Point out each Plasmodium parasite.
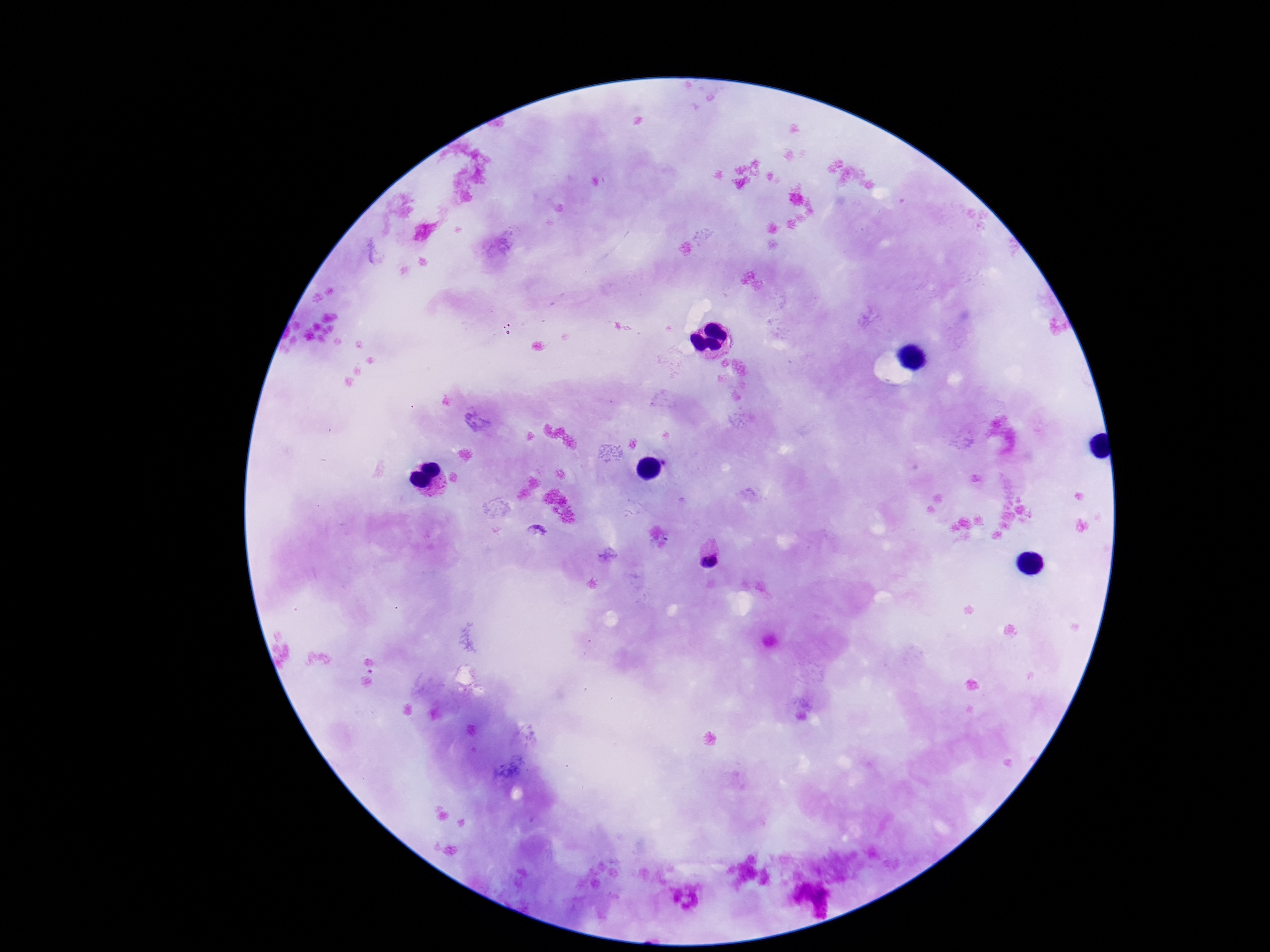
Approximate object centers, in pixels from the top-left corner.
Plasmodium parasites: (x=710, y=557).

magnification = 100x
stain = Giemsa
capture = smartphone camera through the microscope eyepiece
field of view = single
image size = 1270×952 pixels
preparation = thick peripheral-blood smear
patient malaria status = infected